Classify this cell by malaria status.
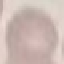

It is uninfected.

Summary:
  - Stain: Giemsa
  - Capture: smartphone through the microscope eyepiece
  - Preparation: thin blood film
  - Image type: automatically extracted cell patch, resized to 64 × 64 pixels